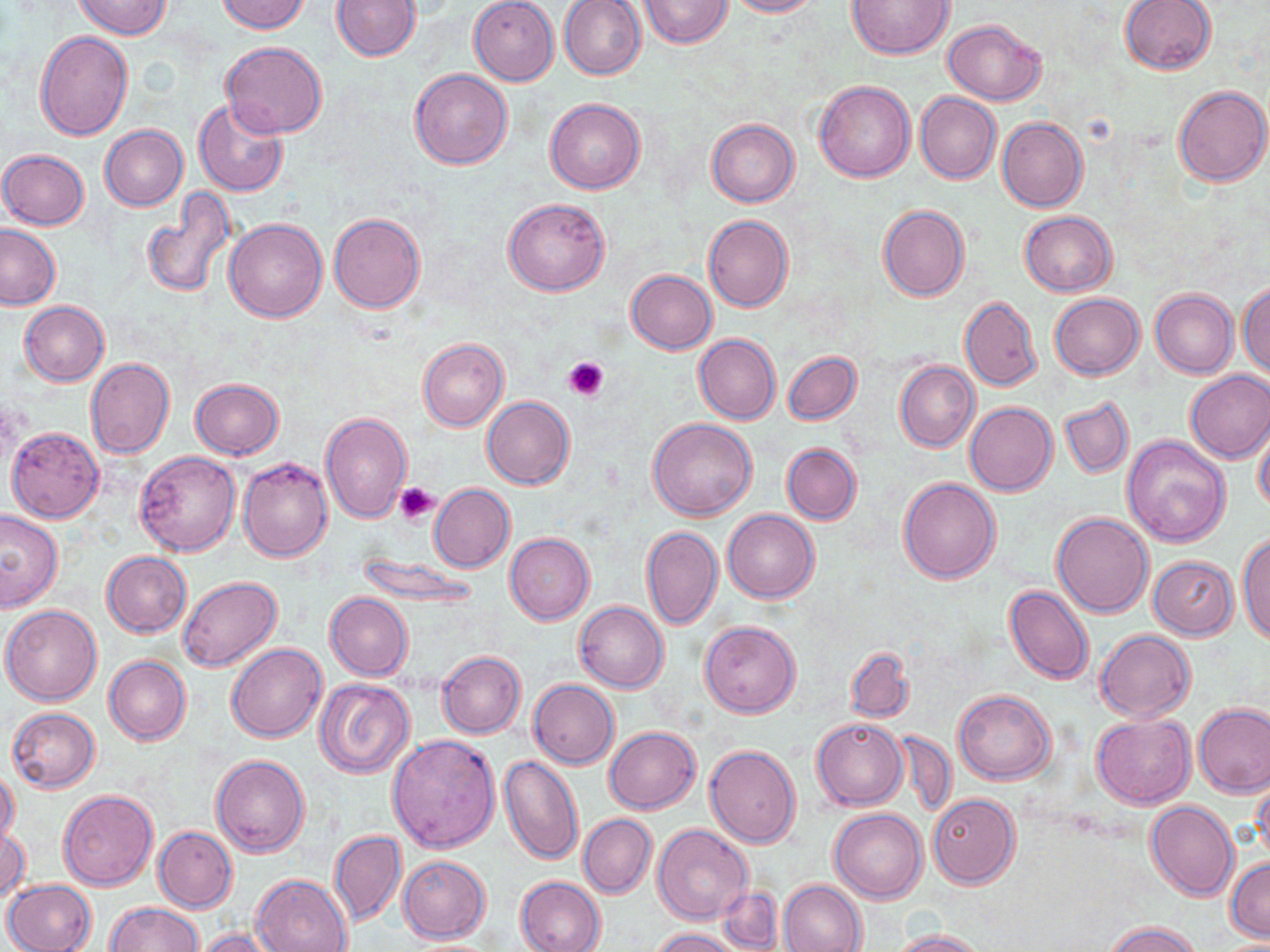
Summary:
  - Coordinate format: approximate bounding boxes as (x1, y1, x2, y2) in pixels
  - Platelet locations: (564, 355, 609, 400), (395, 483, 439, 525)
  - Uninfected red blood cell locations: (217, 0, 310, 34), (331, 0, 420, 61), (638, 0, 732, 49), (722, 0, 820, 17), (846, 0, 953, 58), (1119, 0, 1217, 75), (74, 1, 172, 38), (469, 1, 559, 84), (560, 1, 648, 80), (942, 18, 1046, 104), (35, 31, 133, 140), (220, 41, 328, 139), (409, 69, 513, 170), (815, 81, 915, 182), (1172, 85, 1269, 187), (915, 92, 1001, 183), (546, 98, 646, 194), (192, 99, 290, 197), (997, 117, 1088, 212), (707, 118, 800, 207), (100, 124, 189, 211), (0, 149, 90, 230), (139, 188, 236, 300), (503, 198, 611, 296), (878, 205, 969, 300), (1019, 211, 1115, 297), (328, 212, 426, 313), (703, 215, 794, 312), (225, 217, 328, 322), (0, 224, 61, 310), (626, 270, 716, 354), (1238, 281, 1269, 377), (1150, 288, 1237, 378), (1049, 293, 1145, 380), (959, 296, 1041, 391), (19, 302, 110, 386), (694, 333, 780, 424), (417, 337, 509, 431), (783, 351, 862, 426), (86, 358, 175, 459), (895, 361, 980, 452), (1184, 370, 1270, 463), (189, 378, 285, 459), (482, 397, 575, 490), (1059, 398, 1134, 478), (965, 402, 1057, 496), (320, 411, 414, 524), (648, 417, 758, 521), (1254, 421, 1270, 513), (6, 426, 104, 522), (1121, 435, 1231, 546), (782, 444, 862, 525), (133, 451, 240, 556), (239, 457, 333, 564), (898, 477, 1000, 584), (429, 484, 515, 573), (0, 508, 65, 612), (723, 509, 819, 602), (1052, 512, 1154, 617), (641, 525, 722, 629), (505, 532, 595, 624), (1237, 532, 1270, 645), (101, 551, 192, 637), (354, 554, 483, 607), (1149, 555, 1239, 640), (178, 576, 283, 673), (1004, 586, 1094, 685), (325, 592, 413, 682), (575, 601, 669, 693), (1, 605, 102, 705), (699, 620, 801, 719), (1095, 630, 1196, 722), (226, 643, 327, 742), (845, 646, 914, 724), (437, 651, 526, 738), (104, 655, 191, 746), (315, 679, 415, 778), (529, 680, 619, 768), (953, 689, 1056, 785), (1194, 704, 1270, 798), (6, 707, 100, 792), (1092, 714, 1195, 808), (812, 718, 908, 810), (604, 726, 701, 814), (892, 730, 959, 819), (388, 735, 500, 852), (705, 745, 802, 849), (211, 754, 309, 857), (498, 756, 584, 864), (0, 767, 20, 849), (1253, 773, 1270, 864), (57, 789, 158, 890), (928, 794, 1018, 888), (1146, 801, 1240, 901), (830, 808, 926, 903), (578, 815, 656, 898), (1, 825, 30, 904), (653, 825, 752, 926), (153, 826, 237, 912), (329, 829, 407, 928), (397, 856, 490, 942), (1226, 856, 1270, 942), (250, 873, 352, 952), (515, 875, 606, 952), (3, 879, 97, 952), (779, 879, 867, 952), (717, 885, 782, 950), (104, 902, 203, 952), (1101, 922, 1204, 952), (650, 927, 742, 951), (196, 928, 283, 952), (890, 928, 988, 952)
  - Slide-level diagnosis: negative for blood parasites
  - Magnification: 1000x
  - Image size: 1270×952 pixels
  - Modality: optical microscopy
  - Preparation: thin blood smear
  - Stain: May-Grünwald-Giemsa
  - Field of view: one of a larger specimen